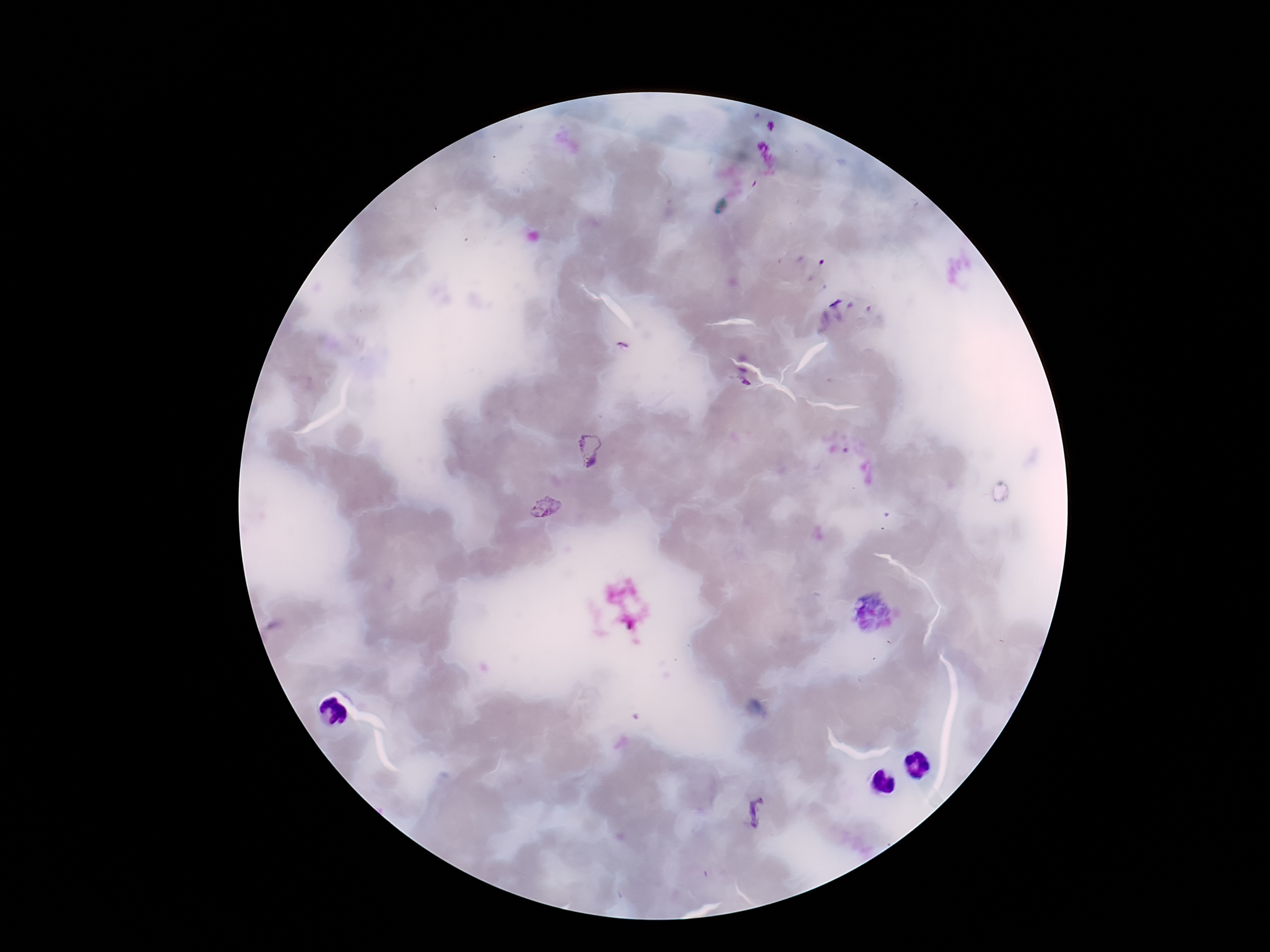
Approximate centers as {x, y} in pixels. Plasmodium parasite locations: {589, 451}, {544, 510}, {757, 812}. Patient malaria status: infected. Thick blood film. Giemsa stain. Image is 1270×952 pixels. Smartphone photograph taken through the microscope eyepiece. 100x magnification. One field from this slide.